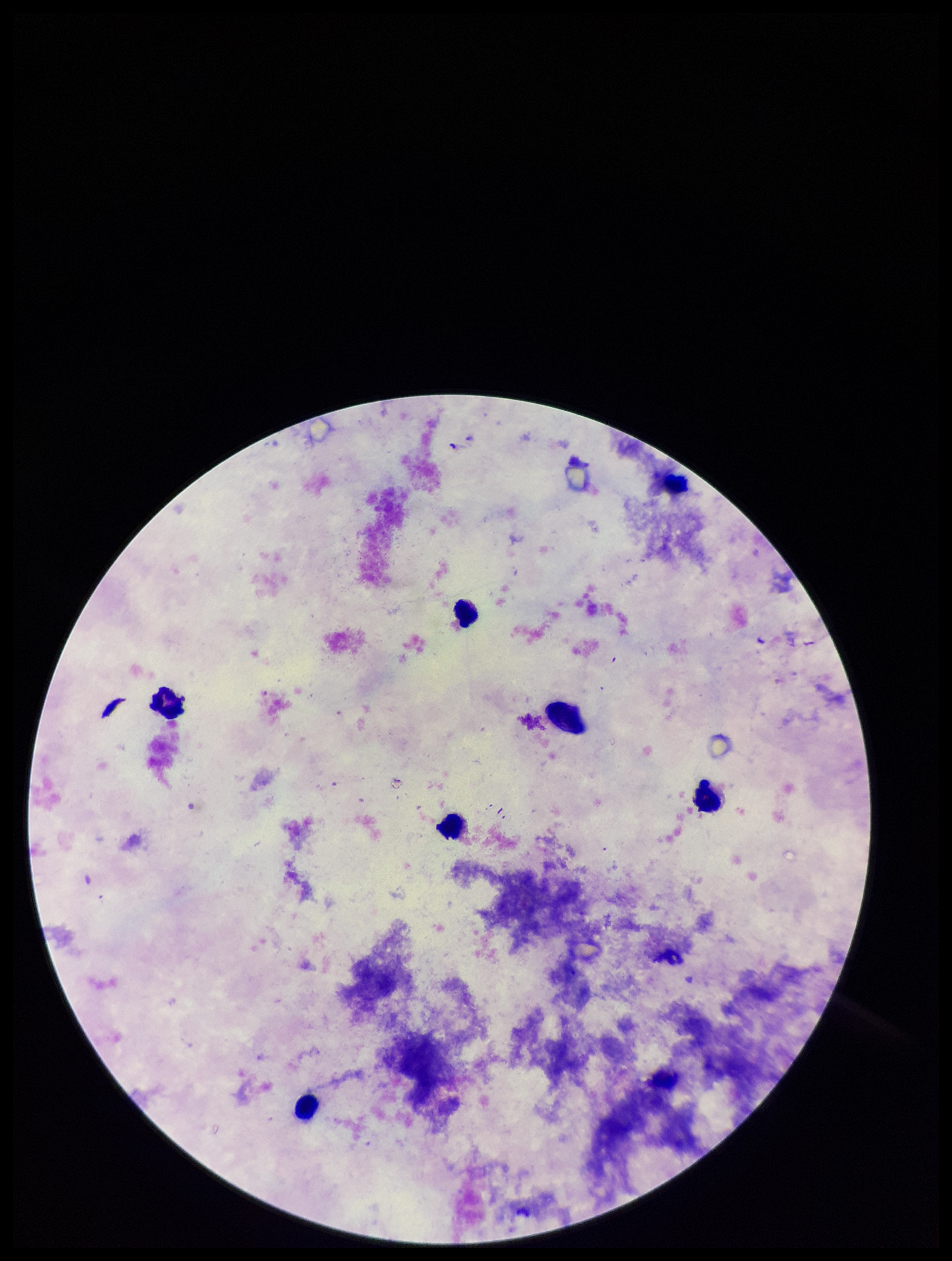
leukocyte count = 6
capture = smartphone photograph through the microscope eyepiece
parasite count = 0
Plasmodium parasites = none seen
image size = 952×1261 pixels
patient malaria status = negative
preparation = thick blood smear
stain = Giemsa
field of view = single